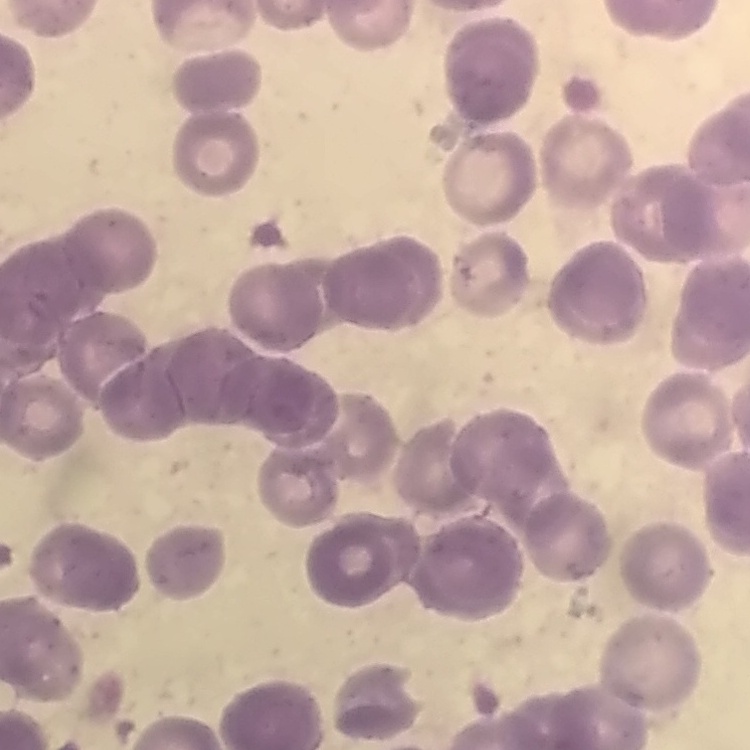
The erythrocytes show rouleaux formation. Square crop of a larger photomicrograph. Field's or Giemsa stain. Thin blood smear.